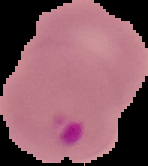
Malaria status: parasitized. From a thin blood smear. Image is 148×166 pixels. The area outside the segmented cell region is set to black.